Give the position of every malaria parasite and every leukocyte.
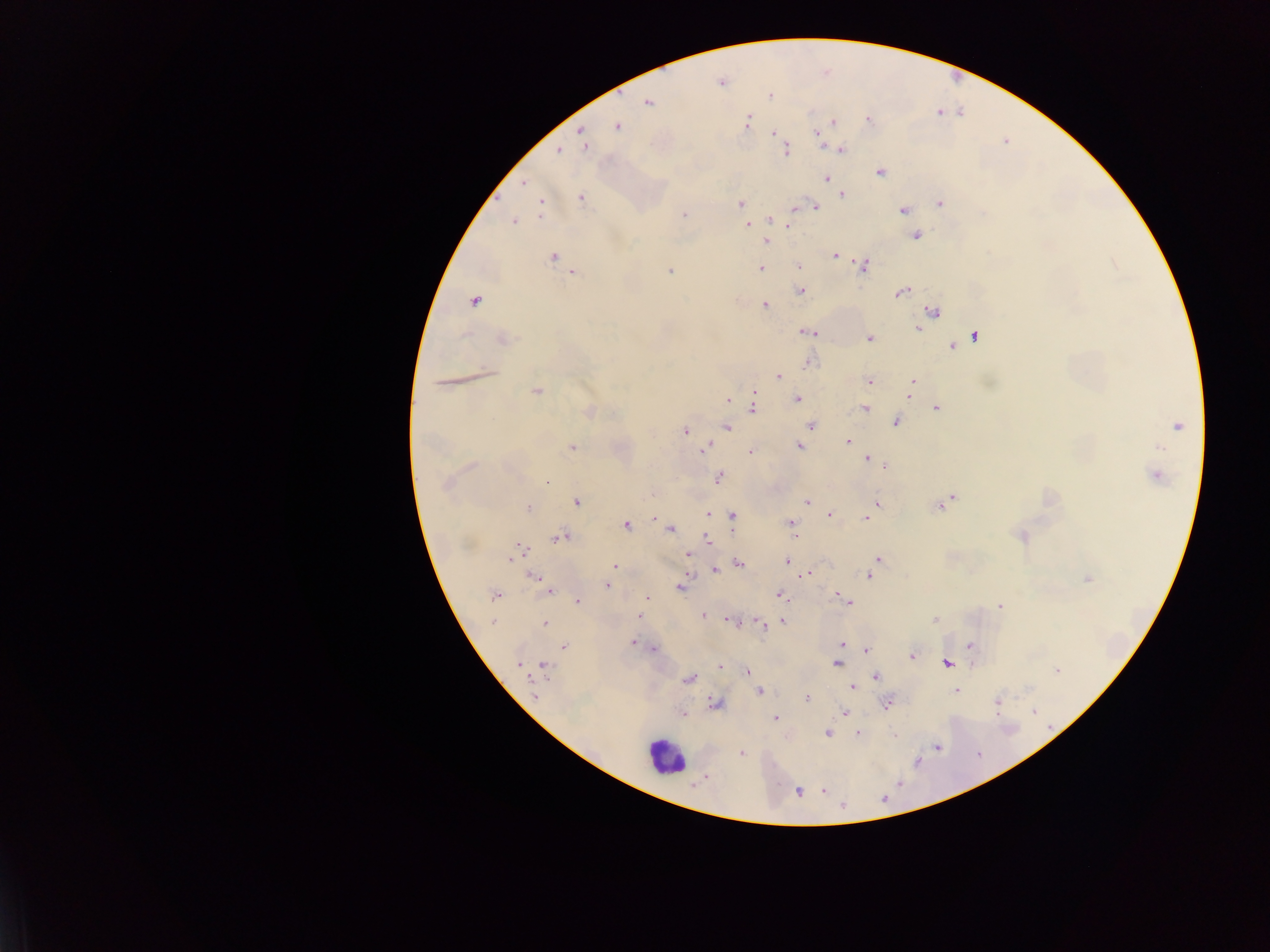
Approximate centers as (x, y) in pixels.
Malaria parasites: (721, 82), (770, 95), (648, 102), (869, 120), (832, 121), (746, 122), (617, 125), (819, 130), (582, 131), (773, 132), (584, 145), (841, 148), (557, 150), (786, 150), (879, 172), (826, 178), (524, 183), (841, 194), (581, 197), (740, 203), (939, 203), (541, 204), (815, 207), (903, 209), (684, 215), (769, 218), (513, 221), (748, 224), (789, 225), (916, 235), (765, 241), (835, 255), (552, 256), (863, 265), (798, 266), (760, 267), (670, 271), (572, 272), (801, 291), (902, 292), (473, 301), (765, 304), (933, 311), (927, 315), (916, 328), (806, 331), (812, 333), (974, 335), (869, 338), (503, 339), (961, 340), (952, 346), (807, 360), (779, 376), (913, 381), (869, 382), (442, 383), (910, 389), (536, 390), (754, 392), (909, 395), (796, 398), (727, 400), (754, 402), (864, 408), (936, 408), (751, 409), (589, 413), (896, 422), (810, 425), (1178, 425), (726, 426), (685, 431), (848, 442), (798, 446), (571, 447), (705, 447), (750, 451), (867, 458), (885, 464), (1155, 475), (718, 477), (547, 482), (446, 483), (652, 492), (575, 501), (807, 502), (942, 502), (877, 503), (527, 508), (709, 514), (715, 514), (828, 514), (731, 517), (654, 518), (866, 518), (791, 522), (625, 525), (670, 528), (794, 532), (1021, 536), (559, 538), (707, 539), (516, 551), (687, 554), (877, 558), (788, 560), (738, 563), (614, 566), (713, 569), (807, 573), (868, 575), (534, 577), (1087, 578), (607, 585), (680, 586), (549, 591), (837, 593), (779, 594), (494, 595), (646, 598), (842, 598), (577, 600), (848, 602), (999, 606), (702, 614), (638, 616), (730, 620), (934, 620), (782, 621), (492, 622), (761, 623), (544, 624), (632, 643), (841, 644), (563, 646), (970, 646), (653, 648), (866, 650), (912, 656), (518, 662), (836, 663), (946, 663), (525, 665), (543, 667), (719, 667), (1057, 669), (746, 672), (875, 676), (688, 679), (853, 686), (759, 691), (955, 691), (535, 696), (806, 698), (997, 701), (887, 703), (715, 704), (845, 712), (682, 714), (774, 718), (827, 732), (856, 733), (894, 734), (939, 747), (741, 753), (704, 777), (823, 789), (797, 792).
Leukocytes: (665, 757).

Summary:
  - Preparation: thick blood film
  - Field of view: single
  - Capture: mobile-phone photograph through a microscope
  - Image size: 1270×952 pixels
  - Country: Ghana